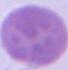
magnification = 1000x
identification = erythrocyte
modality = micrograph